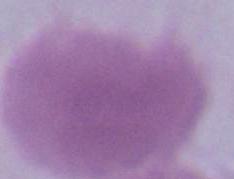
modality: photomicrograph
identification: red blood cell
magnification: 1000x